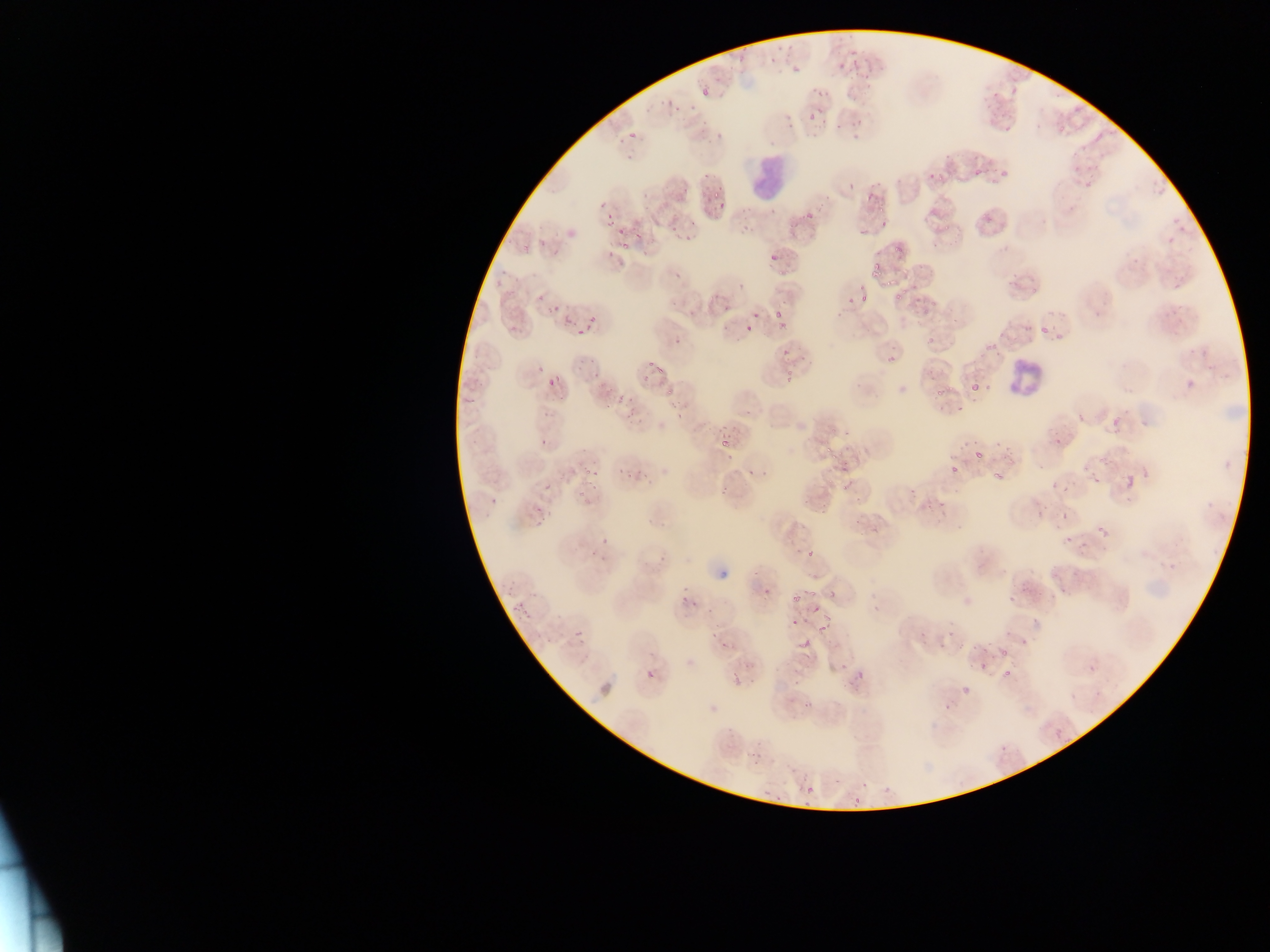

Approximate bounding boxes as left top right bottom in pixels.
Summary:
  - Plasmodium parasite locations: 839 50 860 66; 783 59 807 81; 808 99 839 128; 628 132 637 141; 1096 133 1103 142; 926 168 939 185; 974 169 983 177; 696 181 736 217; 864 182 886 199; 788 207 814 229; 605 215 617 227; 669 219 681 232; 615 235 630 255; 887 235 915 256; 767 244 785 268; 850 263 889 315; 708 270 745 300; 898 273 923 296; 530 294 563 329; 913 297 943 319; 769 299 795 327; 736 310 766 337; 566 322 590 341; 1040 326 1048 334; 925 327 947 345; 772 349 793 363; 638 359 662 387; 778 368 798 383; 547 375 561 390; 970 383 979 392; 618 385 635 399; 933 385 943 396; 614 405 642 433; 718 426 740 450; 812 427 855 464; 1050 428 1070 448; 966 441 983 458; 564 444 594 473; 618 459 655 484; 945 461 961 476; 992 469 1014 486; 1125 476 1135 488; 542 481 553 492; 577 483 594 508; 1059 513 1066 522; 1097 525 1107 537; 800 537 823 559; 670 592 701 613; 791 592 797 603; 809 593 822 612; 705 620 734 646; 812 623 837 636; 573 628 585 640; 917 633 930 653; 973 634 1020 673; 801 638 811 649; 842 652 880 687; 712 654 738 672; 1088 664 1096 672; 645 669 656 680; 944 670 988 708; 1055 730 1063 739; 804 785 814 795; 853 797 861 805 | approximate x y pixel centers of objects too small to bound: 855 137
  - Leukocyte locations: 744 152 794 200; 1004 357 1044 407
  - Capture: mobile-phone photograph through a microscope
  - Country: Ghana
  - Field of view: single
  - Preparation: thin blood smear
  - Image size: 1270×952 pixels